Classify this cell by malaria status.
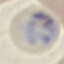

Parasitized.

preparation: thin blood smear
stain: Giemsa
capture: smartphone through the microscope eyepiece
image_type: automatically extracted cell patch, resized to 64 × 64 pixels